Name the cell type shown.
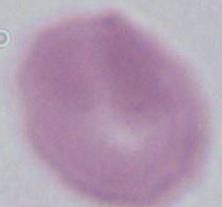
This is an erythrocyte.

Summary:
  - Magnification: 1000x
  - Modality: photomicrograph